Locate every blood parasite and identify its species.
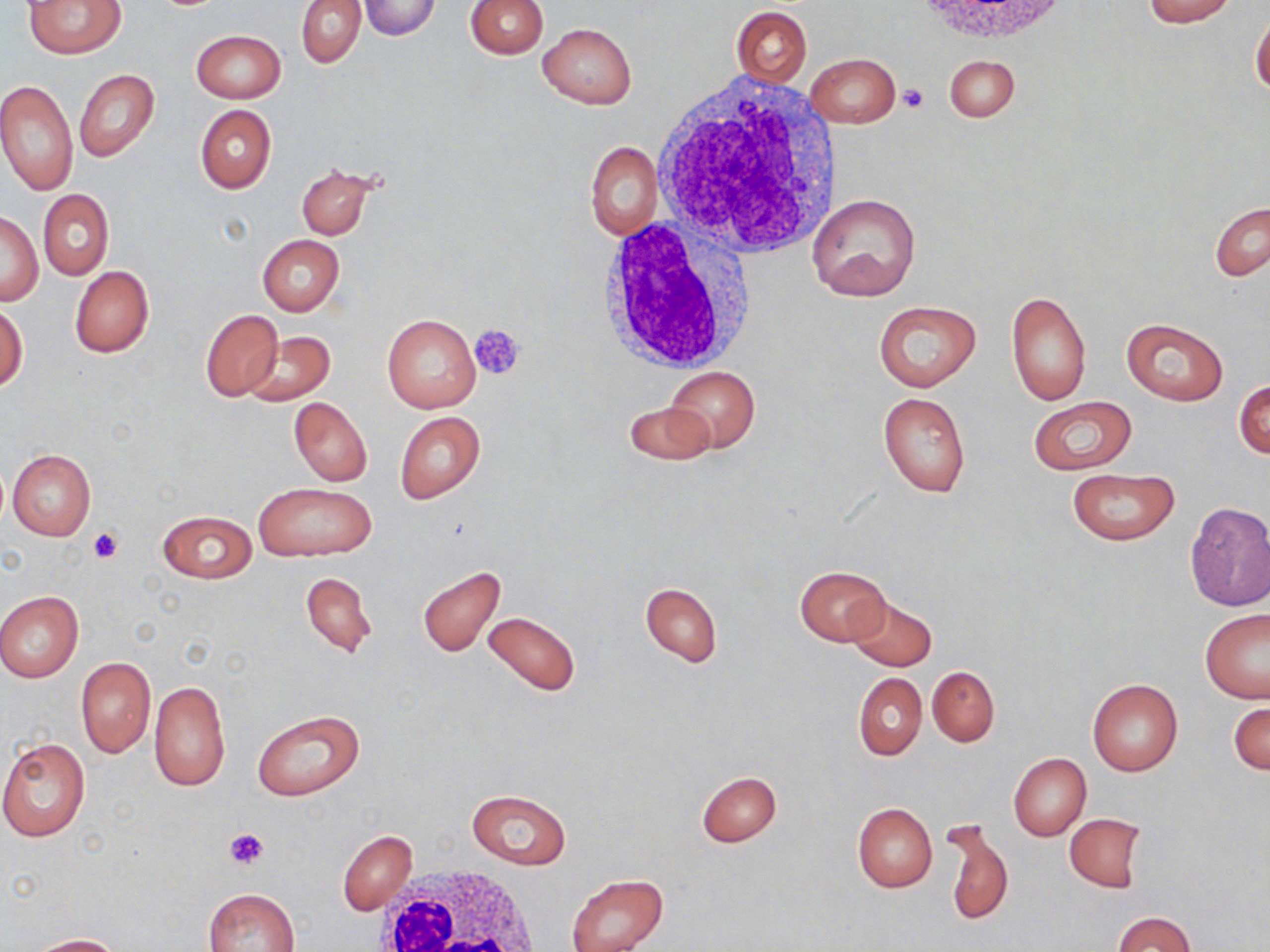

No blood parasites seen.

{
  "slide_level_diagnosis": "negative for blood parasites",
  "platelet_locations": "approximate bounding boxes as named x1/y1/x2/y2 corners in pixels: (x1=898, y1=83, x2=929, y2=113), (x1=470, y1=324, x2=526, y2=381), (x1=88, y1=526, x2=123, y2=563), (x1=224, y1=827, x2=269, y2=870)",
  "magnification": "1000x",
  "stain": "May-Grünwald-Giemsa",
  "modality": "optical microscopy",
  "white_blood_cell_locations": "approximate bounding boxes as named x1/y1/x2/y2 corners in pixels: (x1=650, y1=74, x2=845, y2=260), (x1=592, y1=216, x2=756, y2=375), (x1=370, y1=867, x2=545, y2=952)",
  "preparation": "thin blood smear",
  "uninfected_red_blood_cell_locations": "approximate bounding boxes as named x1/y1/x2/y2 corners in pixels: (x1=24, y1=0, x2=126, y2=57), (x1=296, y1=0, x2=365, y2=67), (x1=465, y1=0, x2=547, y2=58), (x1=1142, y1=0, x2=1238, y2=25), (x1=358, y1=1, x2=442, y2=39), (x1=731, y1=5, x2=811, y2=86), (x1=1250, y1=11, x2=1270, y2=96), (x1=538, y1=23, x2=636, y2=108), (x1=191, y1=29, x2=285, y2=102), (x1=805, y1=53, x2=899, y2=127), (x1=944, y1=55, x2=1018, y2=121), (x1=74, y1=69, x2=158, y2=162), (x1=0, y1=80, x2=77, y2=195), (x1=195, y1=105, x2=275, y2=193), (x1=586, y1=142, x2=662, y2=239), (x1=296, y1=165, x2=379, y2=240), (x1=37, y1=189, x2=113, y2=280), (x1=808, y1=194, x2=922, y2=301), (x1=1209, y1=201, x2=1269, y2=282), (x1=0, y1=212, x2=41, y2=305), (x1=257, y1=235, x2=345, y2=316), (x1=70, y1=265, x2=154, y2=358), (x1=1006, y1=289, x2=1092, y2=407), (x1=0, y1=299, x2=27, y2=392), (x1=873, y1=300, x2=981, y2=390), (x1=199, y1=309, x2=282, y2=401), (x1=382, y1=313, x2=481, y2=413), (x1=1121, y1=318, x2=1230, y2=405), (x1=241, y1=330, x2=335, y2=406), (x1=664, y1=367, x2=760, y2=453), (x1=1235, y1=379, x2=1270, y2=460), (x1=878, y1=391, x2=971, y2=498), (x1=1027, y1=396, x2=1138, y2=475), (x1=288, y1=398, x2=372, y2=486), (x1=624, y1=401, x2=714, y2=466), (x1=395, y1=411, x2=485, y2=503), (x1=6, y1=449, x2=95, y2=542), (x1=1065, y1=469, x2=1179, y2=545), (x1=253, y1=481, x2=375, y2=562), (x1=1183, y1=501, x2=1270, y2=611), (x1=156, y1=510, x2=256, y2=583), (x1=416, y1=565, x2=507, y2=657), (x1=795, y1=565, x2=890, y2=645), (x1=301, y1=573, x2=377, y2=656), (x1=640, y1=583, x2=721, y2=666), (x1=0, y1=591, x2=84, y2=681), (x1=848, y1=596, x2=937, y2=670), (x1=1200, y1=608, x2=1270, y2=703), (x1=482, y1=609, x2=580, y2=698), (x1=76, y1=656, x2=155, y2=757), (x1=927, y1=665, x2=999, y2=746), (x1=854, y1=673, x2=926, y2=760), (x1=1087, y1=678, x2=1183, y2=776), (x1=148, y1=679, x2=230, y2=792), (x1=1230, y1=700, x2=1269, y2=775), (x1=253, y1=710, x2=363, y2=801), (x1=0, y1=738, x2=90, y2=841), (x1=1008, y1=752, x2=1090, y2=841), (x1=697, y1=770, x2=781, y2=846), (x1=466, y1=789, x2=570, y2=868), (x1=852, y1=802, x2=937, y2=892), (x1=1064, y1=814, x2=1146, y2=892), (x1=942, y1=818, x2=1013, y2=927), (x1=338, y1=830, x2=415, y2=915), (x1=567, y1=874, x2=666, y2=952), (x1=203, y1=888, x2=299, y2=952), (x1=1114, y1=912, x2=1195, y2=952), (x1=26, y1=933, x2=122, y2=951)",
  "field_of_view": "single",
  "image_size": "1270×952 pixels"
}